Assess this cell for malaria.
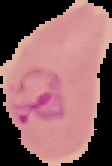
It is parasitized.

Summary:
  - Preparation: thin blood smear
  - Image size: 112×166 pixels
  - Image type: segmented cell region on a black background